Identify the blood parasite species.
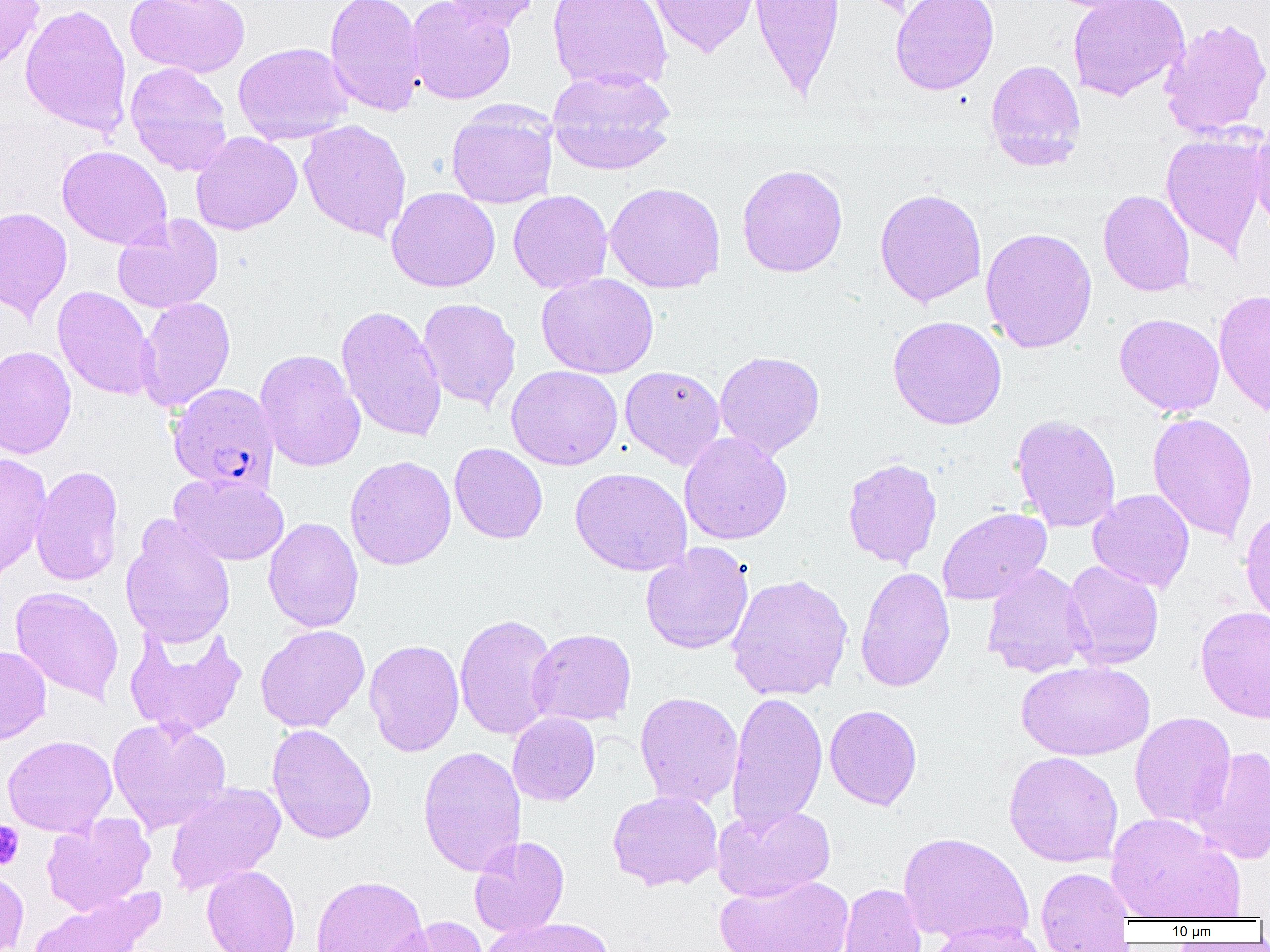

Plasmodium falciparum.

Approximate bounding boxes as (x1,y1)-(x2,y2) corner pairs in pixels. Plasmodium falciparum-infected red blood cell locations: (167,382)-(279,494). Platelet locations: (0,821)-(24,869). Uninfected red blood cell locations: (0,0)-(44,72), (124,0)-(250,78), (324,0)-(425,117), (406,0)-(516,105), (438,0)-(542,32), (547,0)-(673,92), (648,0)-(761,58), (748,0)-(846,101), (891,0)-(999,95), (1067,0)-(1190,101), (20,4)-(133,137), (1159,17)-(1270,138), (233,42)-(353,145), (985,59)-(1086,171), (125,61)-(232,176), (547,68)-(677,174), (446,105)-(557,209), (298,119)-(412,241), (1249,120)-(1270,235), (191,131)-(302,235), (1161,131)-(1268,256), (56,145)-(172,250), (736,163)-(848,277), (605,182)-(726,293), (386,187)-(500,293), (874,188)-(988,307), (508,190)-(613,293), (1098,190)-(1195,297), (0,206)-(72,321), (112,214)-(224,314), (980,226)-(1098,353), (536,273)-(659,379), (52,286)-(156,400), (1214,289)-(1270,416), (136,297)-(236,412), (417,298)-(521,411), (336,304)-(447,443), (1114,313)-(1225,416), (887,315)-(1007,430), (0,345)-(77,459), (255,349)-(366,472), (714,350)-(825,459), (506,365)-(622,470), (619,365)-(726,469), (1147,412)-(1258,543), (1011,414)-(1122,533), (679,432)-(792,545), (449,442)-(548,544), (0,452)-(52,582), (344,455)-(457,570), (842,457)-(942,569), (31,464)-(124,587), (570,467)-(691,576), (169,473)-(289,565), (1088,489)-(1195,593), (937,507)-(1052,606), (1239,507)-(1270,627), (120,516)-(236,648), (263,517)-(363,632), (640,543)-(754,655), (1062,560)-(1164,670), (981,563)-(1094,678), (854,566)-(955,692), (726,573)-(853,701), (10,586)-(124,704), (1194,605)-(1270,724), (454,613)-(559,741), (124,621)-(247,741), (255,624)-(370,733), (527,628)-(637,726), (364,639)-(465,756), (0,645)-(51,745), (1016,660)-(1155,761), (635,691)-(743,808), (726,691)-(828,834), (824,704)-(922,810), (508,712)-(600,806), (1130,712)-(1236,828), (107,717)-(232,834), (267,724)-(377,844), (2,735)-(117,837), (417,746)-(526,877), (1190,746)-(1270,864), (1003,750)-(1123,867), (165,782)-(286,895), (607,789)-(724,891), (712,803)-(835,902), (1106,812)-(1243,921), (42,813)-(156,915), (898,831)-(1034,945), (469,836)-(570,938), (202,864)-(300,952), (1035,866)-(1136,950), (0,867)-(29,952), (311,874)-(429,952), (715,874)-(854,952), (838,883)-(928,952), (30,888)-(165,952), (381,916)-(488,952), (480,916)-(615,952), (923,922)-(1047,952). Image is 1270×952 pixels. Thin blood smear. One field of a larger specimen. Captured at 1000x magnification. Optical microscopy.